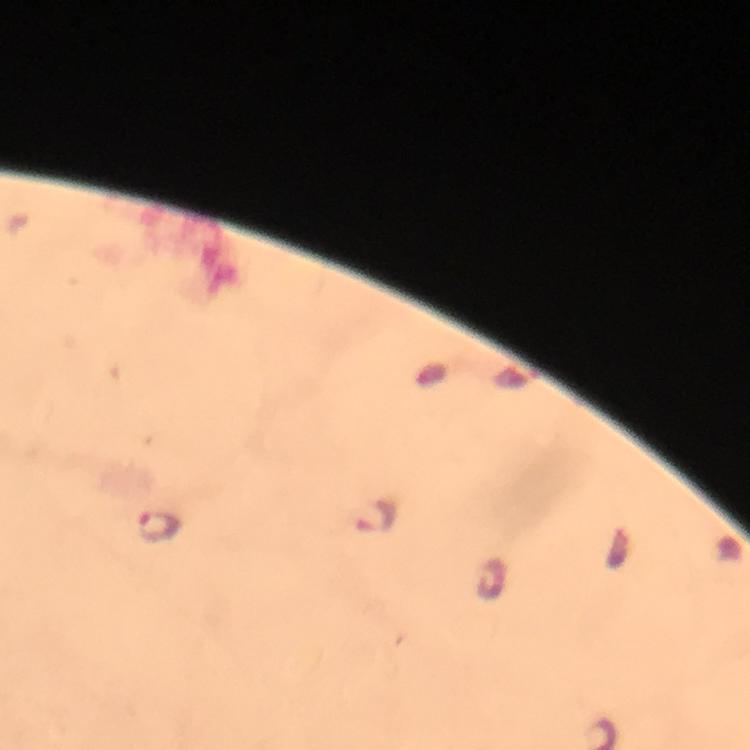

Approximate object centers, in pixels from the top-left corner.
Summary:
  - Malaria parasite locations: (x=375, y=516), (x=157, y=526)
  - Immersion oil: used
  - Magnification: 100x
  - Preparation: thick blood film
  - Stain: Giemsa
  - Context: from a diagnostic examination for malaria
  - Capture: smartphone photograph through a microscope
  - Image size: 750×750 pixels
  - Cropped from: a single field of view